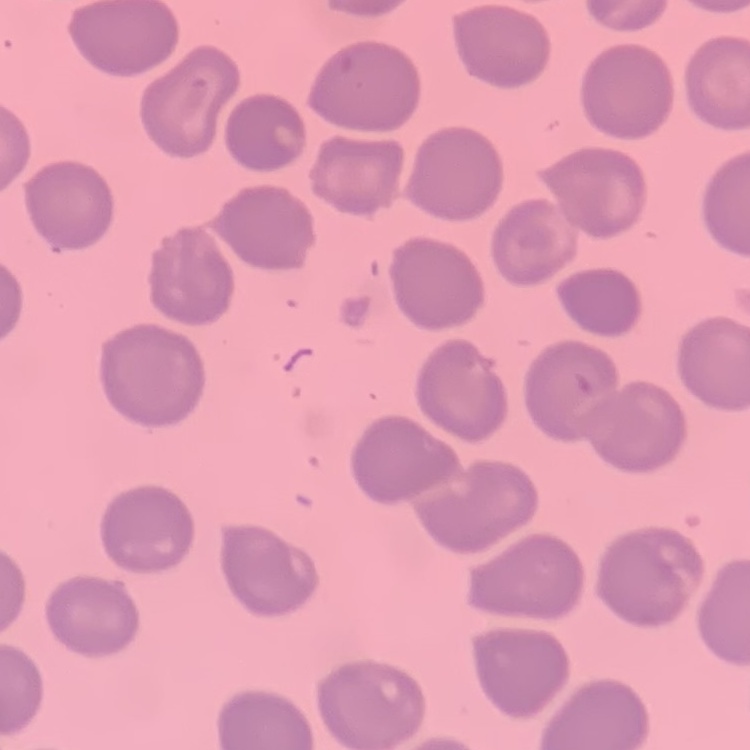
The erythrocytes show no rouleaux formation. Field's or Giemsa stain. Thin peripheral smear. One tile cut from a larger photomicrograph.